Name the blood parasite species.
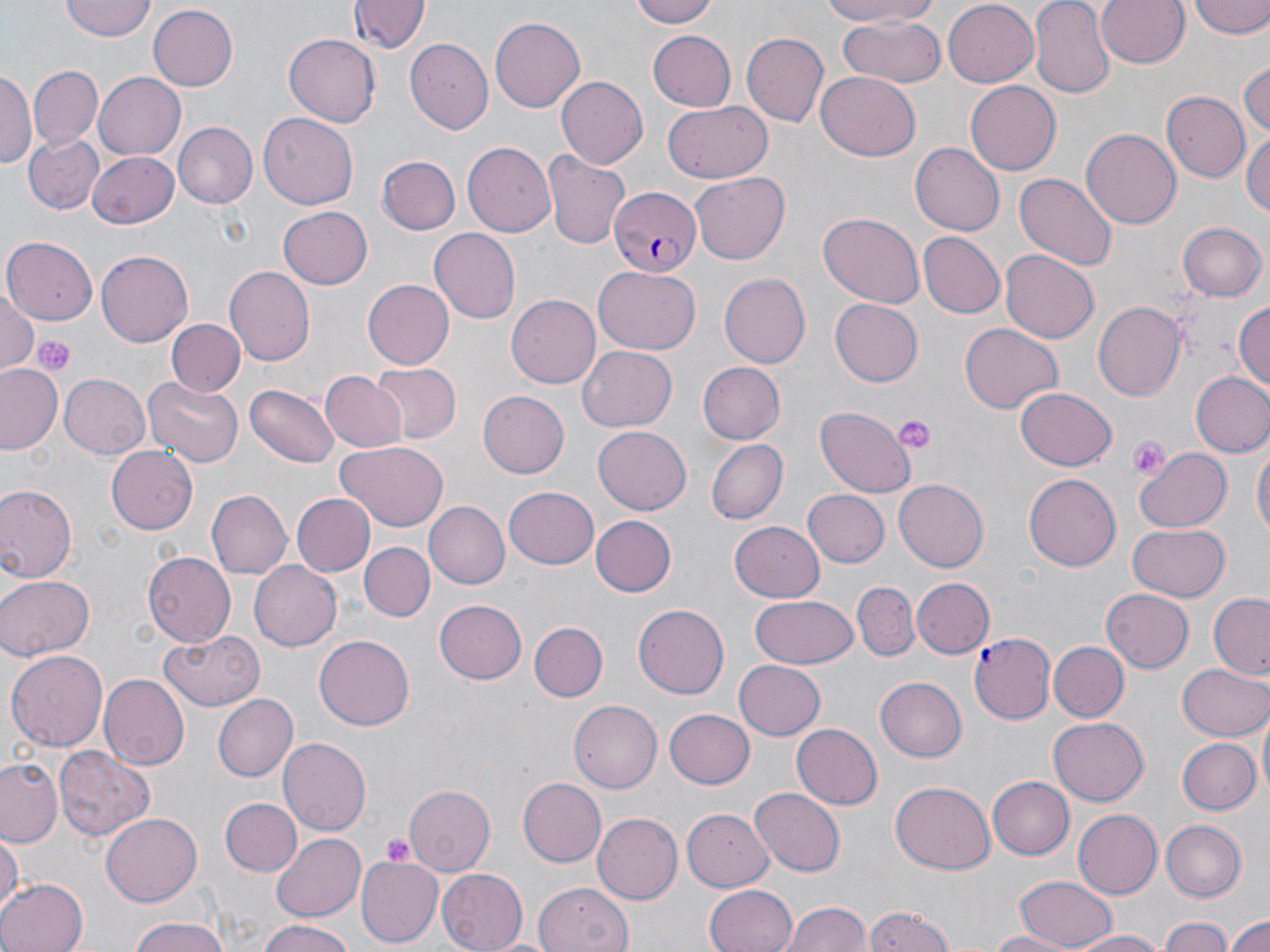

Plasmodium falciparum.

image size = 1270×952 pixels
uninfected red blood cell locations = approximate bounding boxes as named x1/y1/x2/y2 corners in pixels: (x1=60, y1=0, x2=156, y2=42), (x1=627, y1=0, x2=726, y2=27), (x1=811, y1=0, x2=944, y2=26), (x1=1030, y1=0, x2=1115, y2=98), (x1=1095, y1=0, x2=1190, y2=69), (x1=351, y1=1, x2=428, y2=54), (x1=942, y1=1, x2=1040, y2=87), (x1=1188, y1=1, x2=1270, y2=40), (x1=148, y1=5, x2=238, y2=90), (x1=835, y1=12, x2=947, y2=90), (x1=488, y1=16, x2=587, y2=114), (x1=647, y1=31, x2=735, y2=111), (x1=739, y1=32, x2=828, y2=127), (x1=282, y1=34, x2=379, y2=127), (x1=404, y1=38, x2=491, y2=135), (x1=1239, y1=59, x2=1270, y2=140), (x1=30, y1=65, x2=101, y2=148), (x1=0, y1=69, x2=35, y2=171), (x1=817, y1=70, x2=919, y2=160), (x1=93, y1=72, x2=186, y2=161), (x1=556, y1=76, x2=649, y2=169), (x1=963, y1=79, x2=1060, y2=173), (x1=1162, y1=91, x2=1248, y2=183), (x1=663, y1=101, x2=773, y2=184), (x1=258, y1=113, x2=360, y2=208), (x1=173, y1=123, x2=257, y2=208), (x1=1082, y1=127, x2=1181, y2=229), (x1=1244, y1=127, x2=1269, y2=217), (x1=25, y1=134, x2=101, y2=215), (x1=462, y1=142, x2=555, y2=238), (x1=911, y1=143, x2=1003, y2=236), (x1=543, y1=148, x2=630, y2=250), (x1=86, y1=152, x2=181, y2=229), (x1=377, y1=156, x2=460, y2=234), (x1=689, y1=171, x2=788, y2=265), (x1=1014, y1=174, x2=1117, y2=272), (x1=277, y1=206, x2=372, y2=289), (x1=819, y1=210, x2=925, y2=307), (x1=1179, y1=222, x2=1266, y2=301), (x1=429, y1=227, x2=522, y2=323), (x1=917, y1=231, x2=1004, y2=318), (x1=1, y1=236, x2=98, y2=324), (x1=96, y1=250, x2=192, y2=344), (x1=1001, y1=250, x2=1099, y2=344), (x1=225, y1=266, x2=314, y2=365), (x1=592, y1=266, x2=701, y2=355), (x1=718, y1=272, x2=812, y2=368), (x1=361, y1=279, x2=455, y2=369), (x1=0, y1=288, x2=38, y2=374), (x1=507, y1=293, x2=602, y2=389), (x1=831, y1=298, x2=923, y2=385), (x1=1233, y1=299, x2=1270, y2=395), (x1=1091, y1=300, x2=1184, y2=401), (x1=165, y1=320, x2=244, y2=396), (x1=959, y1=323, x2=1062, y2=415), (x1=578, y1=346, x2=677, y2=430), (x1=696, y1=361, x2=783, y2=443), (x1=369, y1=362, x2=459, y2=444), (x1=0, y1=364, x2=64, y2=454), (x1=321, y1=370, x2=409, y2=452), (x1=1190, y1=372, x2=1270, y2=457), (x1=60, y1=373, x2=150, y2=458), (x1=142, y1=375, x2=245, y2=468), (x1=247, y1=384, x2=338, y2=468), (x1=1014, y1=387, x2=1118, y2=471), (x1=478, y1=389, x2=569, y2=479), (x1=816, y1=406, x2=915, y2=498), (x1=593, y1=426, x2=690, y2=514), (x1=708, y1=439, x2=786, y2=525), (x1=334, y1=440, x2=448, y2=531), (x1=1253, y1=444, x2=1269, y2=540), (x1=105, y1=445, x2=198, y2=536), (x1=1135, y1=447, x2=1230, y2=535), (x1=1023, y1=471, x2=1120, y2=567), (x1=894, y1=478, x2=989, y2=571), (x1=0, y1=483, x2=78, y2=585), (x1=503, y1=485, x2=599, y2=568), (x1=804, y1=488, x2=890, y2=567), (x1=206, y1=489, x2=291, y2=579), (x1=291, y1=493, x2=375, y2=576), (x1=425, y1=501, x2=510, y2=589), (x1=591, y1=516, x2=677, y2=596), (x1=730, y1=517, x2=827, y2=601), (x1=1127, y1=523, x2=1231, y2=603), (x1=360, y1=542, x2=434, y2=621), (x1=141, y1=550, x2=235, y2=646), (x1=250, y1=562, x2=341, y2=651), (x1=0, y1=573, x2=95, y2=661), (x1=911, y1=576, x2=993, y2=657), (x1=852, y1=581, x2=920, y2=661), (x1=1102, y1=588, x2=1193, y2=673), (x1=749, y1=594, x2=858, y2=670), (x1=1208, y1=595, x2=1269, y2=679), (x1=434, y1=598, x2=528, y2=684), (x1=632, y1=604, x2=729, y2=697), (x1=529, y1=620, x2=606, y2=702), (x1=159, y1=630, x2=265, y2=712), (x1=314, y1=634, x2=415, y2=729), (x1=1048, y1=640, x2=1127, y2=719), (x1=6, y1=649, x2=110, y2=750), (x1=735, y1=660, x2=827, y2=740), (x1=1178, y1=662, x2=1270, y2=742), (x1=101, y1=673, x2=190, y2=770), (x1=875, y1=674, x2=970, y2=762), (x1=215, y1=694, x2=299, y2=782), (x1=568, y1=701, x2=662, y2=791), (x1=1256, y1=706, x2=1269, y2=806), (x1=664, y1=707, x2=754, y2=788), (x1=1049, y1=717, x2=1149, y2=805), (x1=792, y1=724, x2=882, y2=808), (x1=1176, y1=737, x2=1258, y2=815), (x1=278, y1=739, x2=370, y2=836), (x1=55, y1=747, x2=154, y2=841), (x1=0, y1=758, x2=63, y2=846), (x1=987, y1=776, x2=1074, y2=860), (x1=517, y1=778, x2=606, y2=868), (x1=890, y1=781, x2=995, y2=873), (x1=404, y1=783, x2=497, y2=872), (x1=750, y1=787, x2=844, y2=877), (x1=218, y1=798, x2=302, y2=877), (x1=680, y1=808, x2=772, y2=892), (x1=1072, y1=809, x2=1161, y2=899), (x1=592, y1=812, x2=682, y2=903), (x1=102, y1=813, x2=201, y2=906), (x1=1161, y1=819, x2=1246, y2=900), (x1=0, y1=831, x2=24, y2=911), (x1=272, y1=833, x2=366, y2=920), (x1=356, y1=857, x2=443, y2=945), (x1=269, y1=866, x2=362, y2=949), (x1=437, y1=869, x2=528, y2=952), (x1=1015, y1=875, x2=1119, y2=948), (x1=0, y1=877, x2=86, y2=952), (x1=534, y1=880, x2=631, y2=951), (x1=704, y1=883, x2=798, y2=952), (x1=781, y1=901, x2=872, y2=952), (x1=865, y1=907, x2=955, y2=952), (x1=1225, y1=911, x2=1270, y2=952), (x1=1159, y1=916, x2=1235, y2=952), (x1=124, y1=917, x2=234, y2=952), (x1=256, y1=919, x2=354, y2=952), (x1=1065, y1=930, x2=1176, y2=951), (x1=984, y1=931, x2=1078, y2=952)
field of view = one of a larger specimen
platelet locations = approximate bounding boxes as named x1/y1/x2/y2 corners in pixels: (x1=35, y1=336, x2=75, y2=378), (x1=892, y1=415, x2=935, y2=454), (x1=1127, y1=436, x2=1170, y2=478), (x1=380, y1=832, x2=417, y2=867)
magnification = 1000x
modality = light microscopy
Plasmodium falciparum-infected red blood cell locations = approximate bounding boxes as named x1/y1/x2/y2 corners in pixels: (x1=610, y1=189, x2=701, y2=277), (x1=969, y1=632, x2=1054, y2=723)
stain = May-Grünwald-Giemsa
preparation = thin blood film